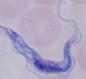
A trypanosome is shown. Micrograph. 1000x magnification.